Describe the morphology of the red blood cells.
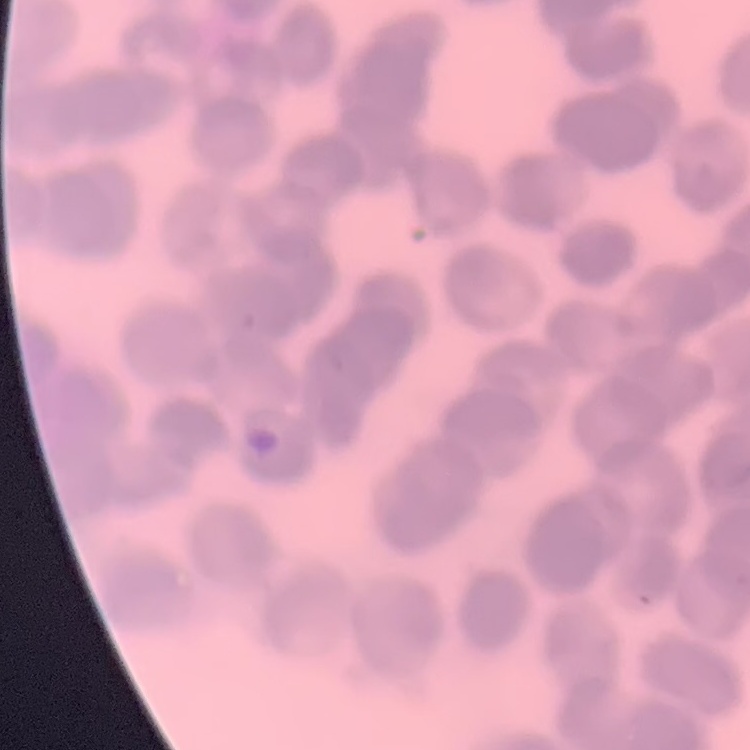
Rouleaux formation.

Square crop of a larger photomicrograph. Stained with either Field's or Giemsa. Thin blood smear.